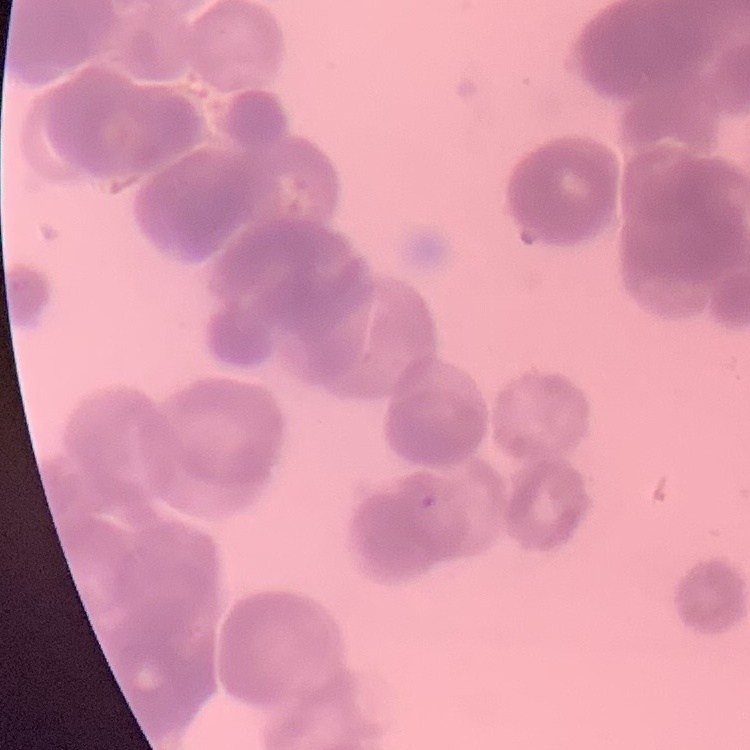
Summary:
  - Erythrocyte morphology: rouleaux formation
  - Stain: Field's or Giemsa
  - Image type: square crop of a larger photomicrograph
  - Preparation: thin blood film